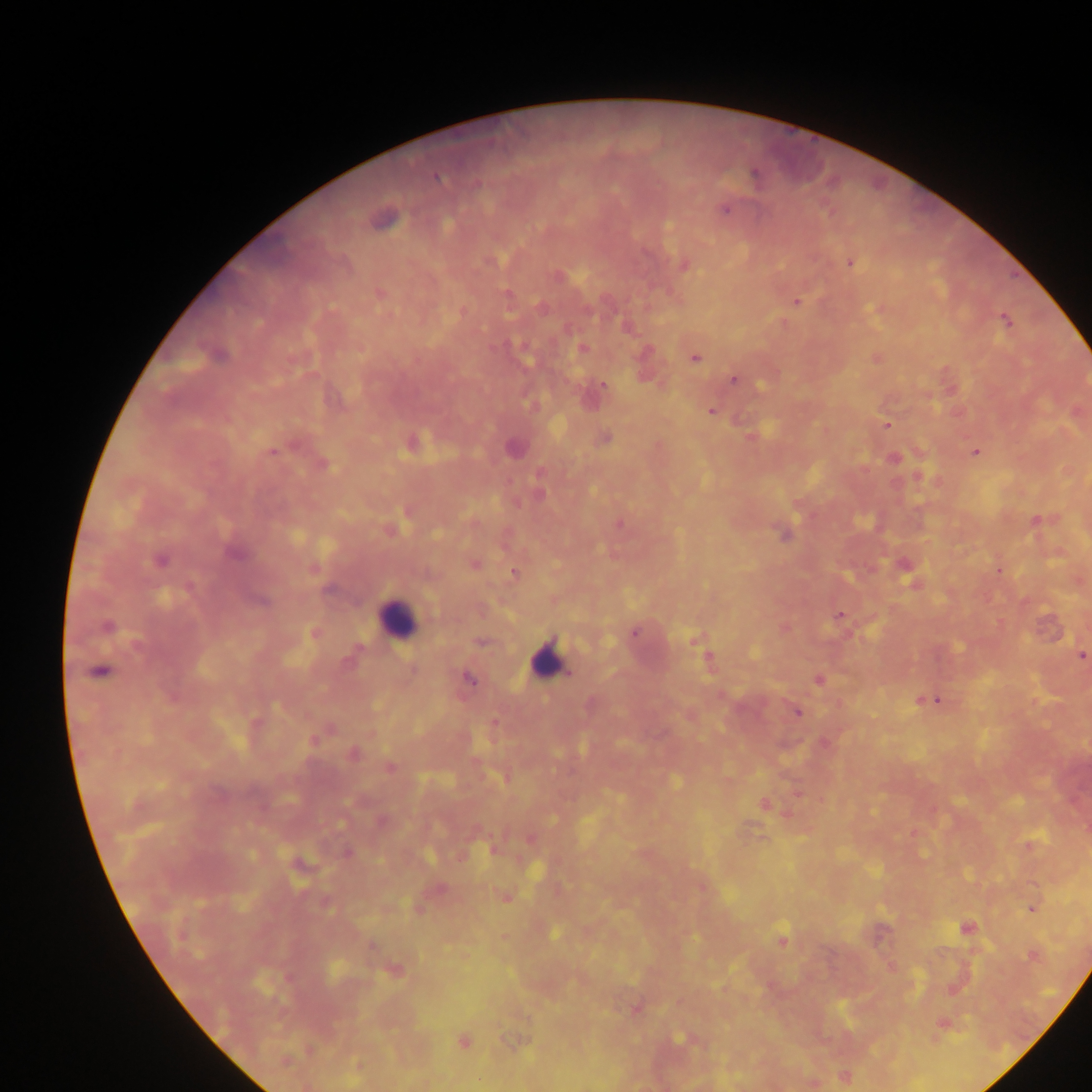 Approximate centers as {x, y} in pixels. Leukocyte locations: {397, 617}, {548, 659}. Plasmodium parasite locations: {754, 174}, {436, 178}, {724, 210}, {383, 220}, {491, 261}, {850, 263}, {685, 265}, {558, 276}, {379, 293}, {796, 302}, {540, 308}, {1006, 320}, {582, 349}, {219, 355}, {695, 358}, {734, 380}, {603, 385}, {712, 411}, {887, 425}, {605, 438}, {514, 448}, {273, 451}, {976, 451}, {322, 464}, {539, 494}, {1035, 519}, {619, 524}, {784, 536}, {234, 553}, {160, 560}, {474, 565}, {514, 573}, {262, 602}, {840, 614}, {106, 626}, {634, 634}, {695, 640}, {481, 642}, {1081, 656}, {708, 658}, {100, 671}, {470, 679}, {819, 680}, {936, 701}, {797, 713}, {314, 739}, {353, 753}, {390, 768}, {765, 804}, {347, 853}, {327, 905}, {1033, 907}, {966, 927}, {554, 933}, {783, 940}, {1033, 956}, {395, 971}, {680, 1038}, {463, 1041}. Thick blood smear. Image is 1092×1092 pixels. Collected in Ghana. Mobile-phone photograph taken through the microscope. One field of view.